Assess this cell for malaria.
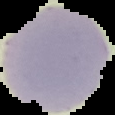

It is uninfected.

Segmented cell region on a black background. From a thin blood smear. Image is 115×115 pixels.